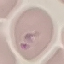
Summary:
  - Result: malaria parasites identified
  - Image type: cell patch, automatically extracted from a larger field of view and resized to 64 × 64 pixels
  - Preparation: thin blood film
  - Capture: smartphone camera at the microscope eyepiece
  - Stain: Giemsa